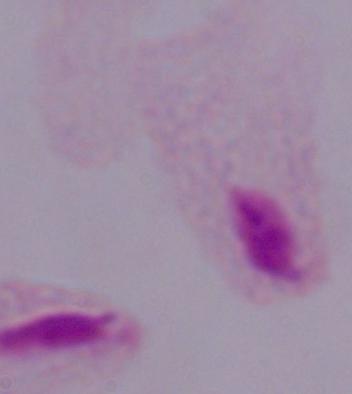
identification = trichomonad
magnification = 1000x
modality = micrograph